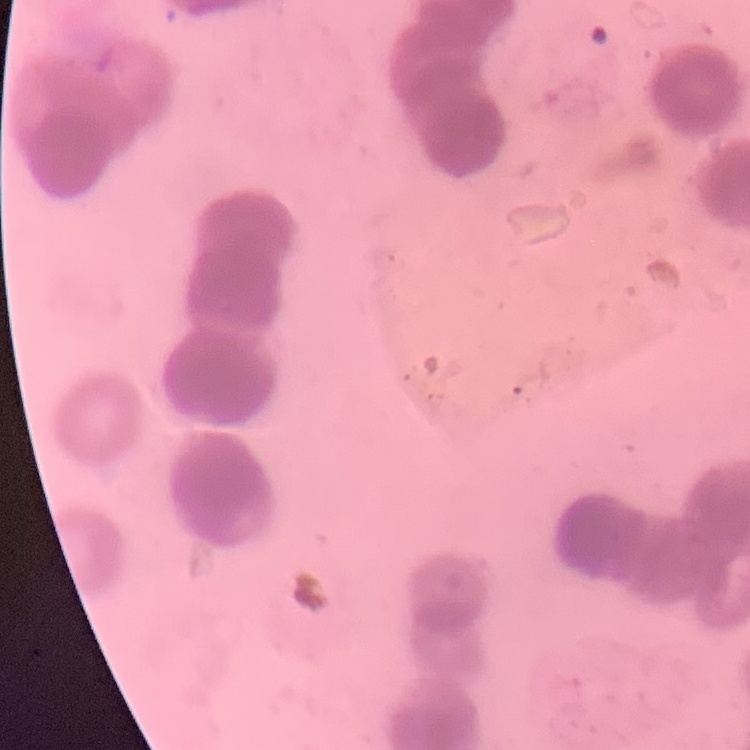 The erythrocytes show rouleaux formation. Field's or Giemsa stain. Thin peripheral smear. Square crop of a larger photomicrograph.